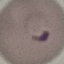

{
  "result": "malaria parasites identified",
  "stain": "Giemsa",
  "preparation": "thin smear",
  "capture": "smartphone through the microscope eyepiece",
  "image_type": "automatically extracted cell patch, resized to 64 × 64 pixels"
}